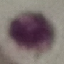

Malaria status: uninfected. Cell patch, automatically extracted from a larger field of view and resized to 64 × 64 pixels. Acquired by smartphone through the microscope eyepiece. Giemsa stain. Thin blood smear.